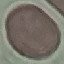
Result: negative for malaria parasites. Automatically extracted cell patch, resized to 64 × 64 pixels. Giemsa stain. Photographed with a smartphone camera at the microscope eyepiece. Thin blood film.